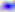

Summary:
  - Magnification: 400x
  - Identification: Toxoplasma gondii
  - Modality: photomicrograph